Give the position of every leukocyte visible.
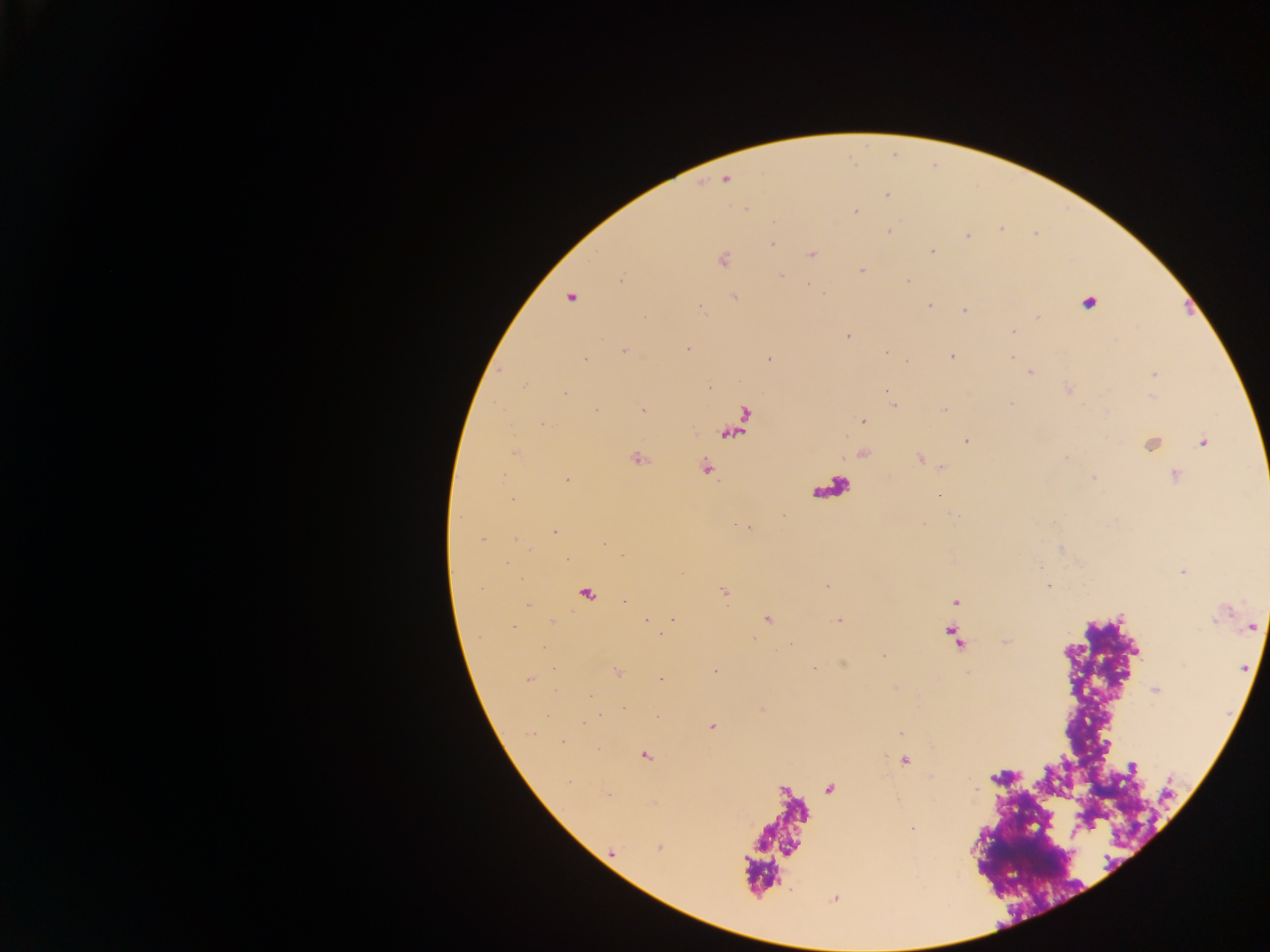
No leukocytes observed.

Approximate centers as {x, y} in pixels. Malaria parasite locations: {725, 180}, {884, 196}, {855, 211}, {1003, 231}, {889, 232}, {967, 236}, {771, 243}, {931, 250}, {812, 254}, {723, 259}, {862, 269}, {782, 274}, {622, 281}, {908, 282}, {735, 297}, {568, 300}, {1088, 303}, {929, 305}, {704, 309}, {963, 310}, {1036, 315}, {1012, 331}, {846, 336}, {688, 348}, {624, 351}, {884, 352}, {951, 356}, {769, 358}, {1011, 358}, {584, 359}, {1029, 372}, {1153, 374}, {526, 383}, {1068, 391}, {566, 392}, {894, 405}, {643, 407}, {596, 408}, {944, 408}, {862, 421}, {543, 425}, {964, 439}, {1202, 442}, {1151, 444}, {513, 450}, {862, 454}, {638, 457}, {1068, 457}, {919, 458}, {705, 466}, {941, 467}, {503, 474}, {1174, 475}, {1093, 477}, {566, 479}, {939, 495}, {783, 514}, {954, 517}, {924, 523}, {738, 524}, {744, 527}, {750, 527}, {554, 532}, {515, 539}, {481, 540}, {1059, 548}, {566, 558}, {1183, 572}, {1050, 585}, {724, 592}, {586, 593}, {623, 600}, {955, 601}, {530, 605}, {767, 618}, {672, 619}, {644, 620}, {837, 621}, {552, 622}, {1250, 625}, {661, 631}, {951, 631}, {955, 639}, {1005, 640}, {546, 648}, {882, 655}, {844, 664}, {814, 668}, {717, 671}, {967, 672}, {617, 673}, {660, 677}, {529, 678}, {896, 688}, {1154, 691}, {763, 709}, {599, 715}, {657, 716}, {584, 724}, {711, 725}, {899, 732}, {529, 734}, {563, 742}, {1106, 747}, {645, 755}, {906, 760}, {1129, 768}, {830, 789}, {1031, 823}, {912, 829}, {611, 853}. Thick blood film. Collected in Ghana. One field of view. Image is 1270×952 pixels. Photographed through a microscope with a mobile-phone camera.